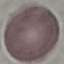
{
  "malaria_status": "uninfected",
  "image_type": "cell patch, automatically extracted from a larger field of view and resized to 64 × 64 pixels",
  "stain": "Giemsa",
  "preparation": "thin blood film",
  "capture": "smartphone camera at the microscope eyepiece"
}